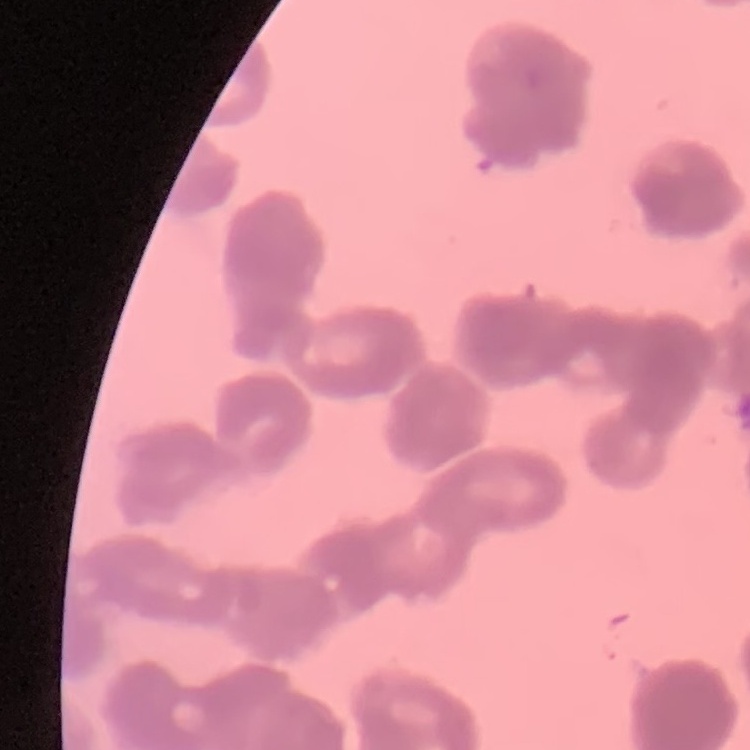
red blood cell morphology = rouleaux formation
stain = Field's or Giemsa
image type = square crop of a larger photomicrograph
preparation = thin blood smear